Classify this cell by malaria status.
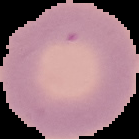

Uninfected.

From a thin blood smear. Image is 139×139 pixels. Cell region segmented out of the field of view; the surrounding area is masked to black.